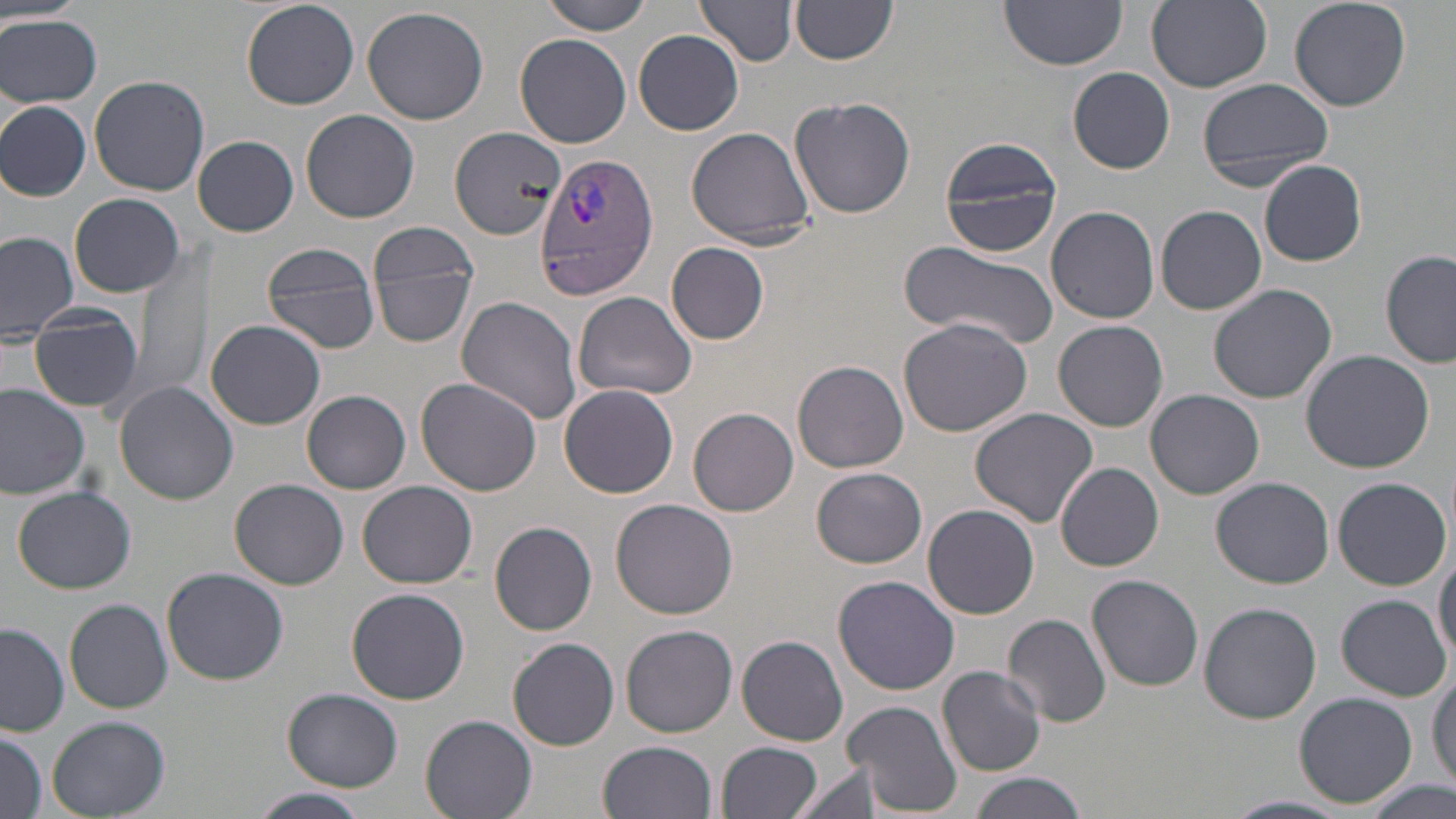
Summary:
  - Coordinate format: approximate bounding boxes as [x1, y1, x2, y2] in pixels
  - Uninfected red blood cell locations: [537, 0, 654, 36], [695, 0, 799, 68], [1000, 0, 1129, 70], [1288, 0, 1413, 112], [240, 1, 358, 110], [791, 1, 900, 66], [1146, 1, 1272, 91], [362, 6, 489, 125], [0, 14, 103, 109], [633, 31, 746, 136], [515, 33, 631, 149], [1068, 67, 1175, 174], [88, 75, 210, 195], [1197, 77, 1335, 190], [789, 96, 915, 218], [0, 101, 91, 202], [301, 109, 420, 223], [449, 125, 567, 241], [684, 127, 816, 248], [193, 135, 299, 237], [938, 137, 1063, 258], [1259, 160, 1367, 267], [70, 192, 186, 297], [1156, 204, 1267, 314], [1046, 205, 1159, 325], [0, 230, 79, 342], [371, 234, 481, 348], [259, 241, 381, 355], [901, 241, 1060, 351], [666, 242, 770, 343], [1380, 250, 1455, 369], [134, 252, 209, 398], [1208, 282, 1339, 404], [571, 290, 696, 402], [456, 295, 585, 425], [30, 305, 143, 412], [898, 317, 1033, 437], [205, 319, 326, 429], [1054, 320, 1169, 431], [436, 325, 571, 476], [1301, 350, 1434, 472], [793, 359, 908, 474], [416, 378, 542, 497], [114, 381, 239, 505], [0, 384, 92, 499], [558, 384, 678, 498], [1145, 389, 1264, 500], [301, 390, 411, 494], [689, 406, 798, 516], [969, 407, 1097, 528], [1056, 463, 1164, 571], [812, 467, 927, 568], [1211, 476, 1334, 588], [1334, 476, 1452, 590], [229, 477, 349, 589], [358, 479, 477, 588], [12, 485, 136, 594], [611, 499, 737, 619], [923, 503, 1041, 619], [490, 521, 597, 637], [1433, 547, 1456, 667], [161, 568, 289, 685], [1086, 574, 1204, 691], [833, 575, 960, 695], [347, 587, 471, 705], [1338, 594, 1451, 701], [65, 598, 172, 714], [1199, 601, 1323, 723], [1004, 614, 1112, 728], [1, 623, 69, 736], [621, 624, 737, 737], [503, 635, 737, 744], [738, 635, 849, 746], [508, 639, 620, 751], [1429, 664, 1455, 789], [938, 666, 1046, 778], [283, 689, 404, 789], [1294, 692, 1418, 806], [843, 701, 961, 818], [421, 714, 538, 819], [45, 715, 170, 817], [1, 730, 45, 819], [597, 741, 718, 819], [716, 741, 824, 819], [795, 763, 885, 819], [967, 773, 1090, 819], [1366, 780, 1452, 819], [249, 788, 376, 819], [1226, 794, 1350, 817]
  - Plasmodium vivax-infected red blood cell locations: [534, 153, 658, 299]
  - Slide-level diagnosis: Plasmodium vivax
  - Image size: 1456×819 pixels
  - Magnification: 1000x
  - Modality: light microscopy
  - Field of view: single
  - Stain: May-Grünwald-Giemsa
  - Preparation: thin blood film